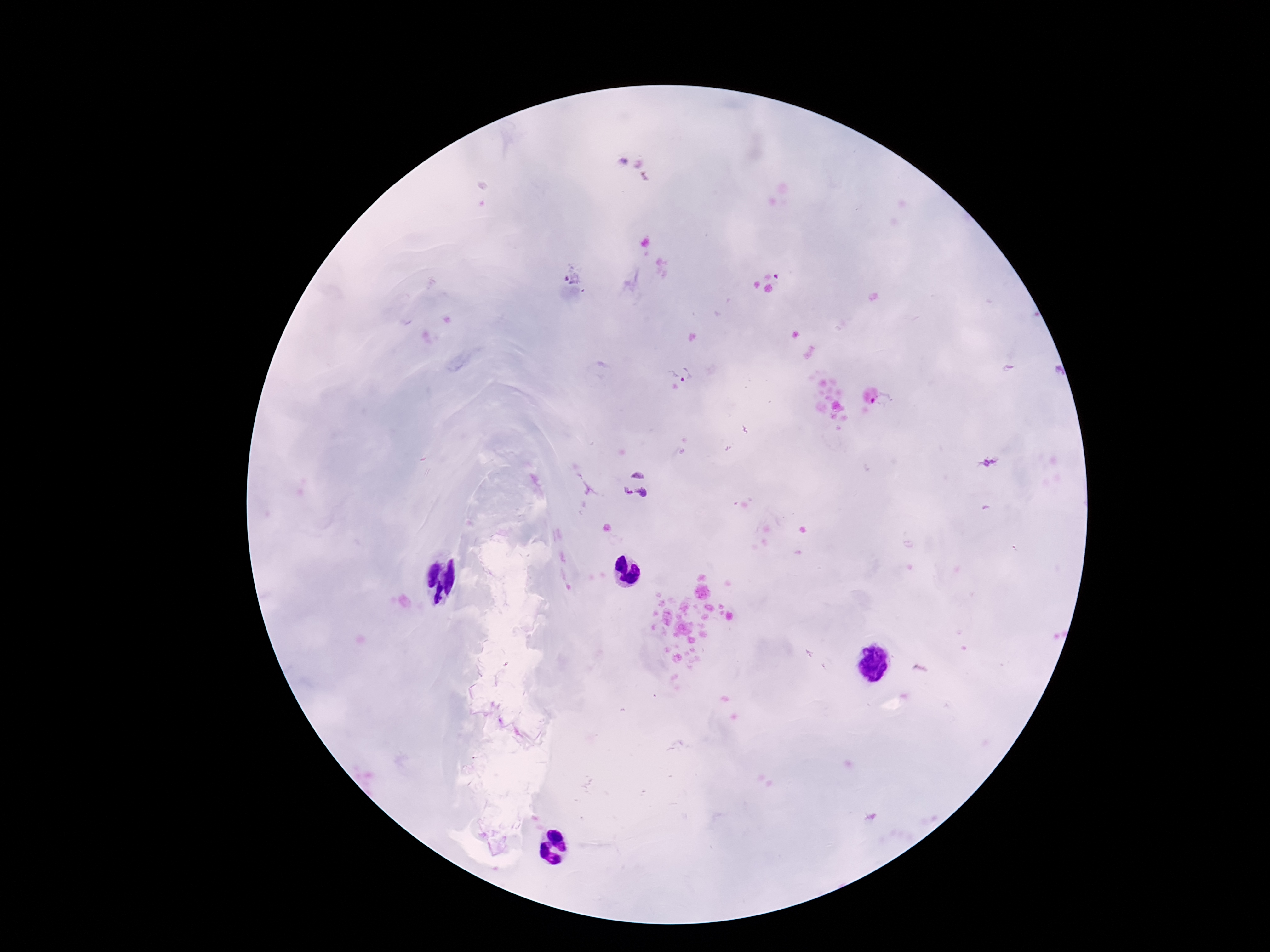

Approximate object centers, in pixels from the top-left corner.
Summary:
  - Plasmodium parasite locations: (x=573, y=270), (x=777, y=276), (x=680, y=371), (x=882, y=400), (x=987, y=464), (x=635, y=486)
  - Patient malaria status: positive
  - Image size: 1270×952 pixels
  - Preparation: thick blood smear
  - Magnification: 100x
  - Field of view: single
  - Stain: Giemsa
  - Capture: smartphone camera through the microscope eyepiece